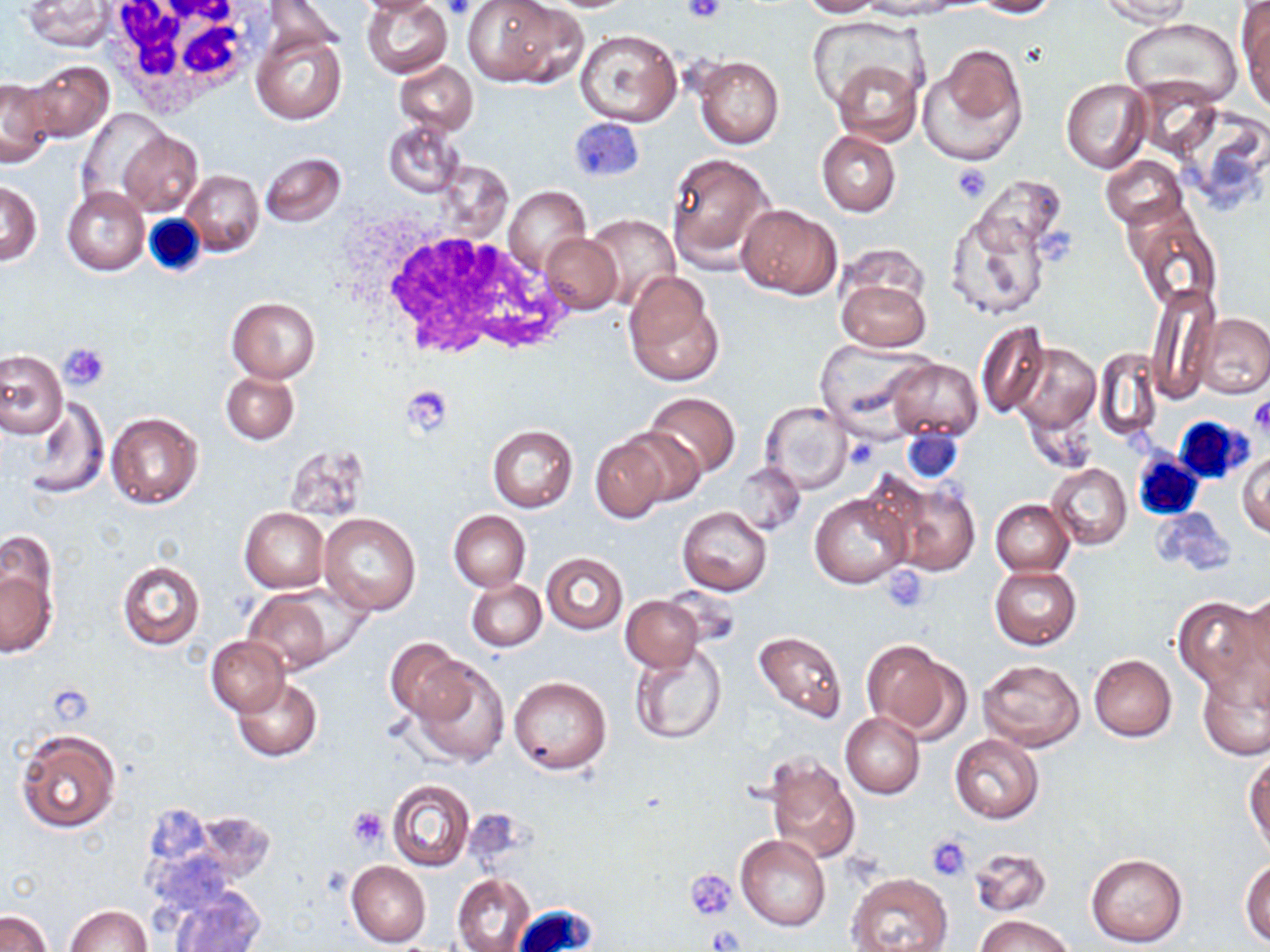
Summary:
  - Coordinate format: approximate bounding boxes as (x1, y1, x2, y2) in pixels
  - White blood cell locations: (96, 0, 266, 117), (143, 214, 207, 278), (364, 224, 575, 361), (1174, 414, 1256, 485), (1132, 454, 1203, 521), (512, 903, 597, 950)
  - Uninfected red blood cell locations: (355, 0, 448, 17), (361, 0, 452, 79), (797, 0, 882, 17), (861, 0, 928, 19), (969, 0, 1058, 17), (21, 1, 114, 52), (462, 1, 582, 88), (1099, 1, 1194, 25), (1238, 5, 1269, 108), (1120, 18, 1242, 109), (573, 28, 682, 127), (250, 30, 345, 124), (919, 43, 1028, 165), (691, 53, 784, 150), (834, 59, 919, 145), (23, 60, 114, 142), (393, 61, 479, 135), (1132, 75, 1223, 158), (0, 78, 57, 166), (1060, 78, 1151, 173), (79, 109, 168, 207), (1178, 113, 1269, 213), (383, 119, 463, 198), (117, 130, 202, 216), (817, 130, 900, 215), (667, 151, 774, 269), (260, 152, 346, 227), (1099, 155, 1188, 228), (180, 169, 263, 257), (974, 174, 1068, 257), (1, 181, 41, 266), (502, 185, 591, 276), (62, 186, 148, 275), (736, 203, 842, 298), (1124, 204, 1221, 313), (944, 208, 1052, 322), (582, 213, 680, 312), (542, 231, 624, 315), (623, 271, 725, 387), (837, 272, 931, 354), (1147, 282, 1219, 400), (227, 297, 320, 382), (1197, 313, 1270, 398), (975, 320, 1049, 417), (813, 340, 936, 435), (1010, 341, 1100, 434), (1092, 349, 1162, 443), (0, 350, 66, 437), (887, 359, 982, 443), (220, 370, 298, 443), (643, 391, 740, 478), (15, 400, 109, 497), (759, 400, 854, 493), (106, 412, 202, 509), (487, 424, 578, 512), (611, 427, 703, 510), (590, 438, 668, 523), (282, 444, 372, 522), (1237, 452, 1270, 537), (731, 462, 806, 534), (1047, 463, 1131, 550), (885, 480, 980, 576), (808, 491, 912, 589), (989, 498, 1074, 576), (677, 506, 772, 596), (1150, 507, 1235, 576), (238, 508, 329, 593), (448, 510, 529, 592), (318, 514, 422, 615), (0, 530, 56, 623), (541, 552, 627, 634), (117, 560, 204, 650), (990, 565, 1081, 650), (2, 569, 55, 656), (466, 578, 546, 652), (240, 590, 345, 675), (1227, 594, 1270, 695), (620, 595, 704, 672), (1174, 596, 1266, 697), (753, 629, 848, 724), (206, 636, 290, 716), (385, 638, 473, 724), (861, 638, 962, 738), (629, 646, 727, 745), (1088, 654, 1177, 741), (978, 657, 1084, 751), (408, 658, 510, 768), (1199, 669, 1269, 759), (509, 675, 612, 775), (232, 677, 323, 761), (840, 713, 925, 798), (16, 728, 120, 833), (949, 735, 1045, 824), (1245, 752, 1270, 853), (763, 755, 860, 864), (387, 779, 474, 871), (192, 811, 275, 884), (736, 835, 830, 931), (970, 847, 1054, 916), (1086, 852, 1188, 947), (1240, 857, 1270, 945), (346, 861, 431, 947), (848, 872, 950, 952), (453, 873, 536, 952), (171, 886, 265, 952), (64, 904, 151, 952), (0, 910, 51, 952), (974, 914, 1076, 952)
  - Platelet locations: (443, 0, 475, 20), (681, 0, 727, 23), (951, 164, 993, 203), (58, 342, 110, 390), (403, 384, 453, 436), (1249, 395, 1270, 436), (844, 439, 877, 470), (884, 567, 931, 611), (348, 806, 388, 849), (926, 834, 972, 880), (686, 868, 738, 919)
  - Slide-level diagnosis: negative for blood parasites
  - Stain: May-Grünwald-Giemsa
  - Image size: 1270×952 pixels
  - Magnification: 1000x
  - Modality: light microscopy
  - Field of view: one of a larger specimen
  - Preparation: thin blood smear